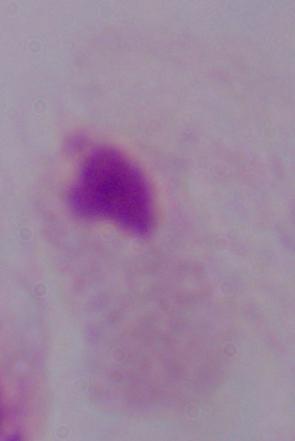
identification = trichomonad
magnification = 1000x
modality = micrograph